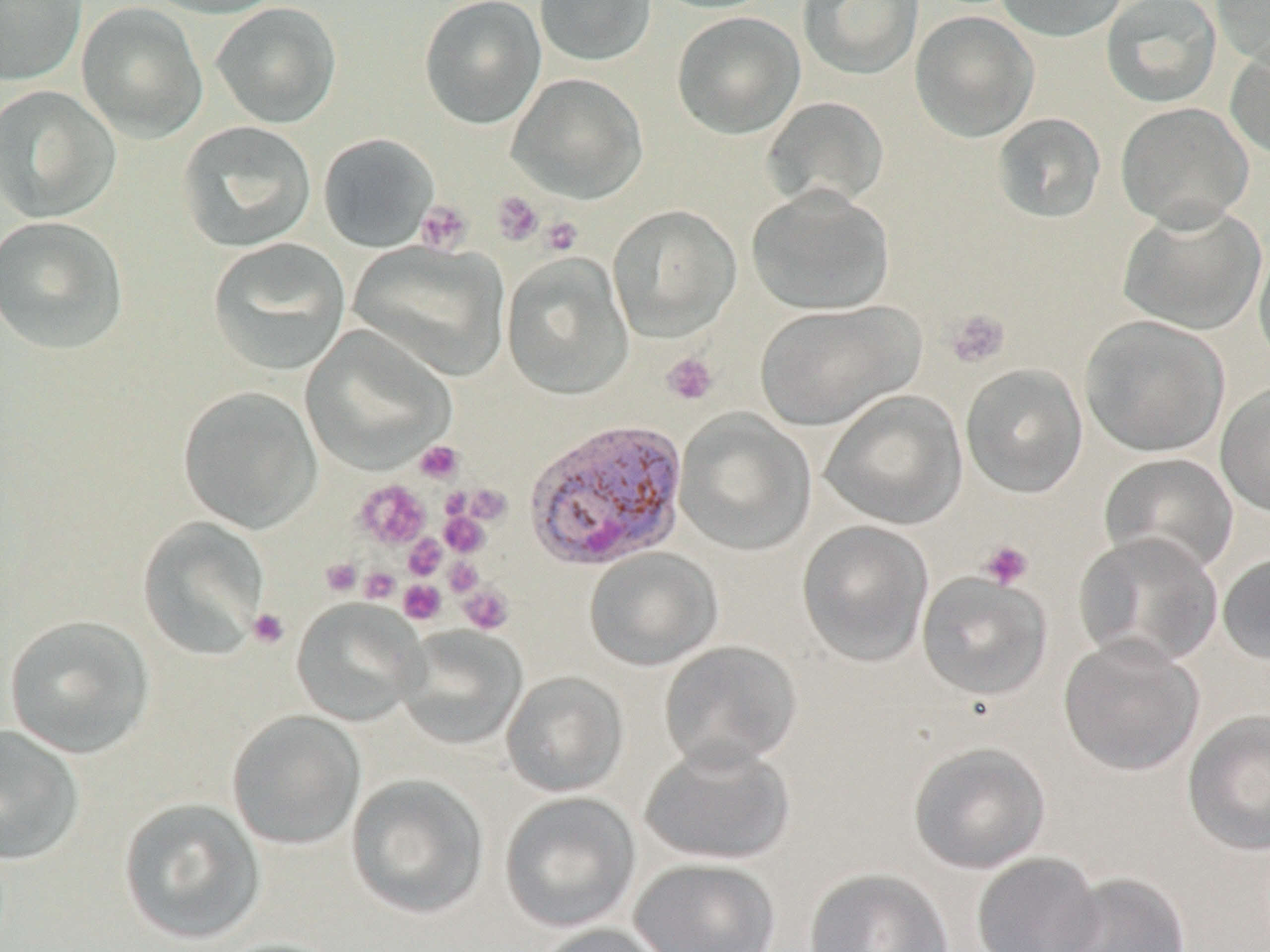
Plasmodium vivax-infected red blood cell locations = approximate bounding boxes as (x1,y1)-(x2,y2) corner pairs in pixels: (526,420)-(691,574)
slide-level diagnosis = Plasmodium vivax
preparation = thin blood smear
stain = May-Grünwald-Giemsa
image size = 1270×952 pixels
magnification = 1000x
modality = light microscopy
uninfected red blood cell locations = approximate bounding boxes as (x1,y1)-(x2,y2) corner pairs in pixels: (0,0)-(87,86), (140,0)-(287,19), (419,0)-(546,129), (534,0)-(656,67), (649,0)-(780,14), (798,0)-(924,80), (992,0)-(1130,42), (1101,0)-(1222,108), (1210,0)-(1270,68), (76,2)-(208,143), (210,2)-(342,129), (672,11)-(805,139), (910,11)-(1039,142), (1225,39)-(1270,161), (507,72)-(648,204), (0,85)-(120,223), (762,96)-(890,212), (1115,102)-(1254,230), (992,113)-(1106,223), (177,120)-(317,252), (318,133)-(439,253), (747,186)-(895,316), (1117,203)-(1267,335), (607,204)-(741,341), (0,215)-(129,354), (207,237)-(351,375), (350,240)-(509,383), (1253,240)-(1270,370), (501,254)-(634,399), (754,299)-(924,431), (1080,315)-(1230,457), (301,325)-(455,474), (961,363)-(1088,498), (1215,381)-(1270,518), (178,386)-(322,533), (820,389)-(968,531), (674,410)-(816,555), (1099,452)-(1239,576), (136,516)-(271,661), (797,520)-(934,667), (1073,531)-(1224,669), (584,547)-(723,671), (1217,551)-(1270,666), (916,571)-(1052,700), (291,598)-(427,726), (4,614)-(155,758), (394,625)-(527,750), (1058,635)-(1205,776), (659,640)-(803,771), (501,671)-(628,797), (226,709)-(366,850), (1182,709)-(1270,856), (0,724)-(85,865), (640,740)-(795,865), (908,740)-(1051,874), (346,773)-(489,920), (499,791)-(641,933), (118,797)-(266,945), (972,851)-(1104,952), (630,857)-(781,952), (804,868)-(953,952), (1052,871)-(1192,952), (532,923)-(671,952), (207,937)-(350,952)
platelet locations = approximate bounding boxes as (x1,y1)-(x2,y2) corner pairs in pixels: (491,191)-(544,246), (415,200)-(473,254), (540,216)-(584,256), (946,308)-(1010,368), (661,352)-(718,406), (414,440)-(463,484), (354,479)-(431,550), (463,484)-(512,525), (440,512)-(489,557), (404,534)-(446,579), (979,540)-(1034,590), (320,557)-(362,597), (443,558)-(483,596), (359,566)-(401,603), (398,579)-(446,625), (458,584)-(514,635), (247,607)-(290,649)
field of view = one of a larger specimen